Locate every blood parasite and identify its species.
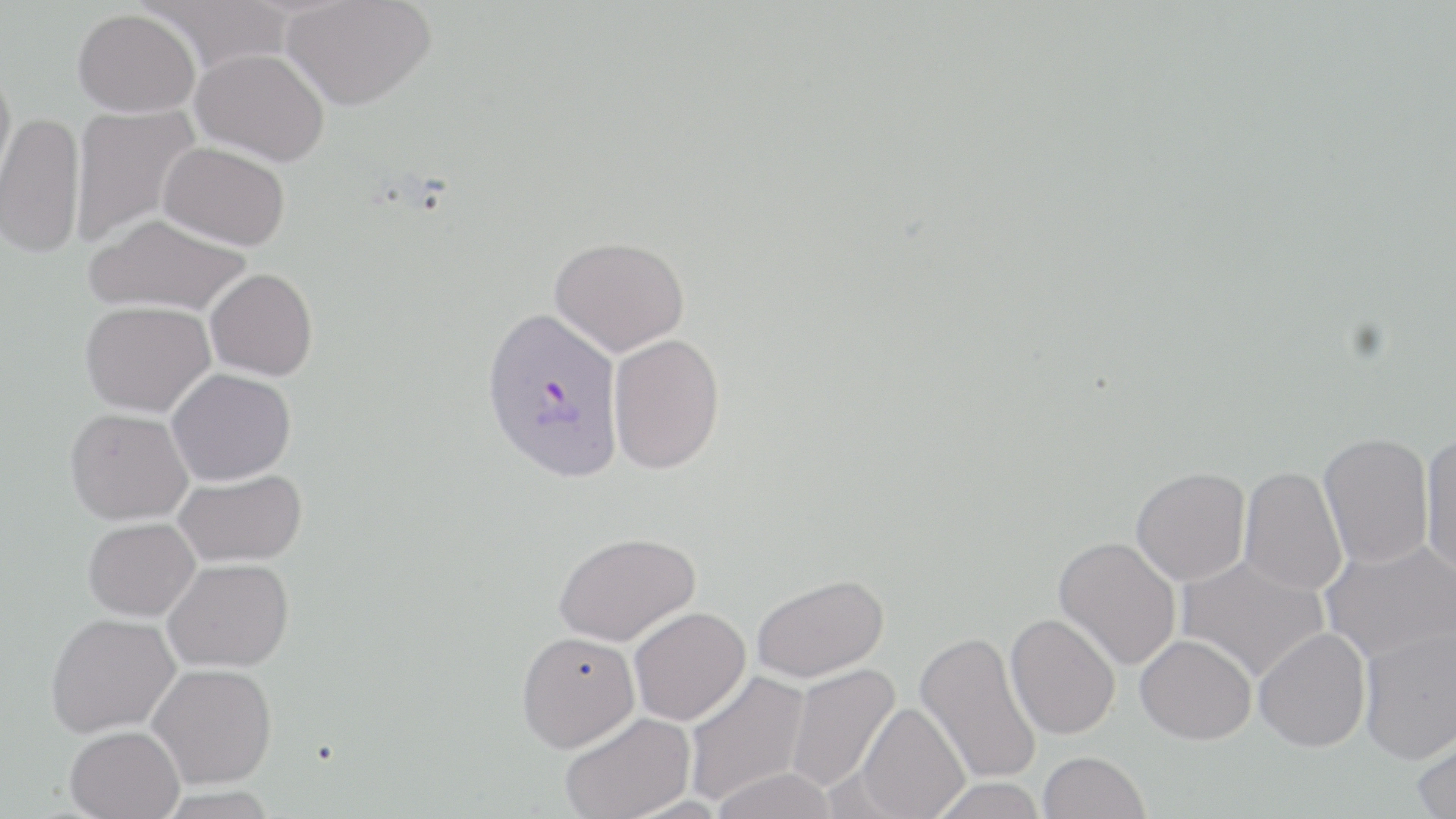

Approximate bounding boxes as [x1, y1, x2, y2] in pixels.
Plasmodium vivax-infected red blood cells: [481, 306, 624, 483].
No Plasmodium falciparum, Plasmodium ovale, Plasmodium malariae, Babesia divergens, or Trypanosoma brucei observed.

Uninfected red blood cell locations: [282, 0, 436, 110], [140, 1, 294, 74], [73, 9, 200, 119], [191, 48, 329, 165], [0, 68, 17, 198], [70, 104, 201, 245], [0, 113, 86, 262], [158, 142, 290, 250], [85, 216, 251, 317], [550, 236, 689, 355], [205, 268, 317, 380], [80, 303, 215, 420], [608, 333, 725, 474], [167, 369, 296, 487], [65, 410, 192, 528], [1420, 432, 1456, 576], [1318, 433, 1434, 569], [1239, 465, 1347, 596], [1131, 467, 1251, 586], [174, 469, 307, 568], [83, 519, 201, 624], [553, 532, 700, 647], [1053, 536, 1182, 671], [1321, 538, 1456, 664], [1175, 553, 1329, 682], [163, 559, 294, 672], [751, 573, 888, 682], [629, 606, 750, 724], [1005, 613, 1121, 740], [46, 615, 180, 739], [1358, 626, 1455, 764], [1254, 627, 1371, 752], [517, 629, 640, 751], [915, 630, 1042, 785], [1136, 634, 1257, 744], [148, 663, 277, 790], [785, 663, 900, 794], [682, 670, 811, 807], [856, 702, 969, 819], [560, 712, 696, 819], [1411, 724, 1456, 819], [65, 728, 185, 818], [1039, 751, 1150, 819], [710, 767, 838, 819], [927, 777, 1049, 818], [155, 786, 279, 819]. Slide-level diagnosis: Plasmodium vivax. Optical microscopy. One field of a larger specimen. May-Grünwald-Giemsa stain. Thin blood film. Captured at 1000x magnification. Image is 1456×819 pixels.